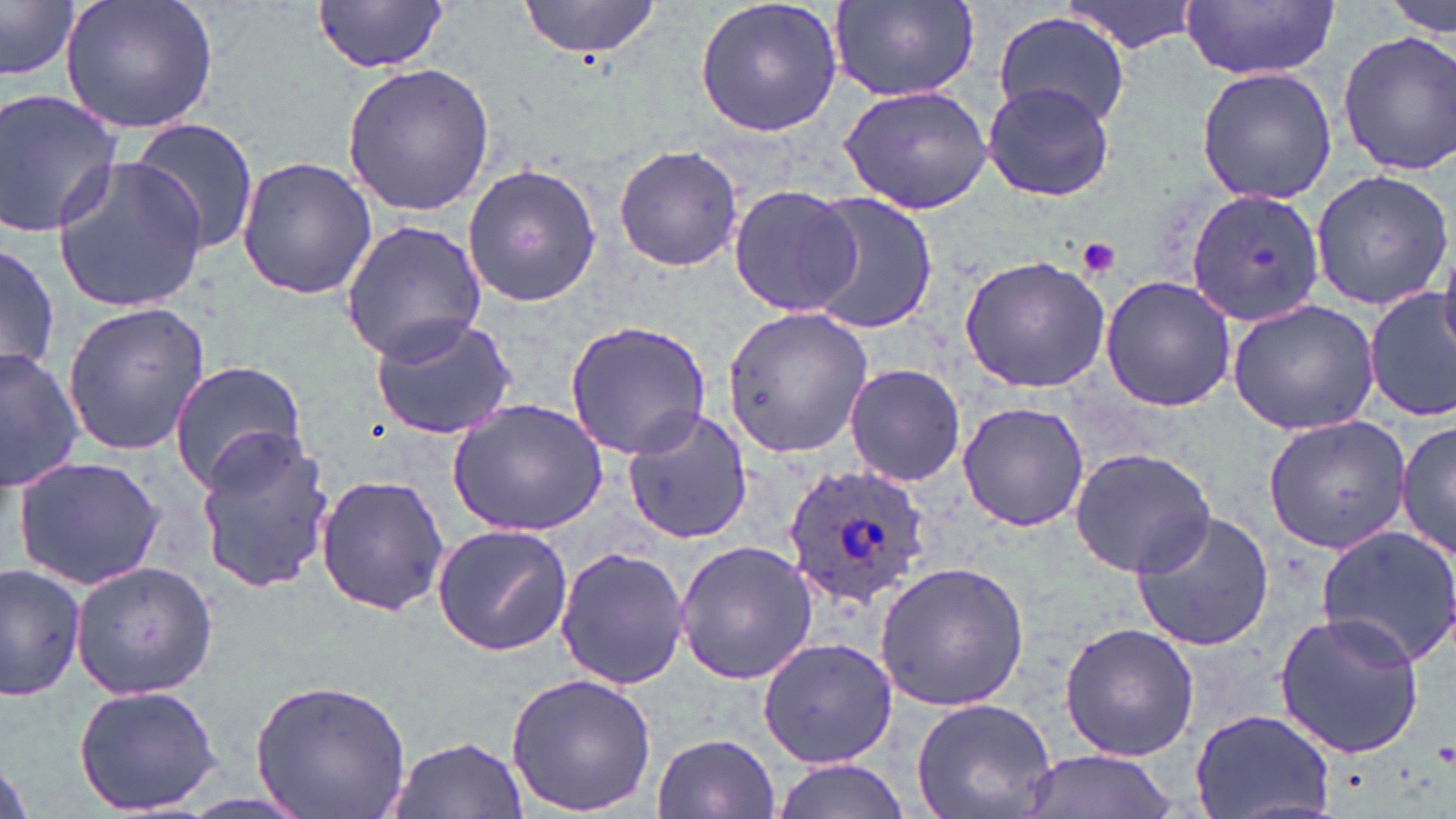 Approximate bounding boxes as (x1, y1, x2, y2) in pixels. Platelet locations: (1077, 237, 1120, 278), (1433, 741, 1456, 768). Uninfected red blood cell locations: (59, 0, 220, 137), (313, 0, 451, 73), (516, 0, 671, 58), (693, 0, 844, 139), (1063, 0, 1200, 54), (1181, 0, 1342, 79), (1384, 0, 1453, 39), (0, 1, 81, 82), (828, 1, 979, 104), (992, 10, 1132, 130), (1337, 32, 1456, 175), (341, 62, 494, 216), (1195, 65, 1335, 205), (839, 78, 997, 215), (982, 81, 1113, 202), (0, 87, 127, 239), (124, 119, 261, 259), (613, 146, 743, 273), (50, 155, 209, 314), (236, 155, 378, 301), (462, 164, 601, 309), (1310, 168, 1454, 312), (727, 185, 861, 317), (1187, 185, 1326, 325), (797, 191, 937, 333), (338, 220, 487, 364), (0, 240, 60, 382), (1436, 248, 1456, 359), (959, 255, 1110, 394), (1100, 277, 1238, 412), (1364, 289, 1455, 423), (1225, 298, 1382, 435), (61, 302, 211, 456), (720, 307, 874, 458), (369, 313, 520, 439), (563, 319, 712, 460), (0, 346, 84, 492), (169, 359, 307, 491), (843, 363, 967, 487), (447, 399, 607, 537), (957, 403, 1091, 532), (619, 408, 752, 548), (1263, 414, 1411, 553), (1397, 416, 1454, 566), (192, 428, 336, 591), (1069, 447, 1215, 575), (12, 455, 167, 591), (315, 474, 449, 617), (1129, 511, 1276, 654), (1313, 520, 1456, 669), (431, 525, 572, 654), (673, 540, 817, 686), (555, 548, 691, 692), (875, 560, 1030, 712), (1, 562, 86, 701), (71, 562, 217, 699), (1273, 611, 1427, 759), (1058, 623, 1200, 763), (758, 637, 897, 768), (505, 672, 658, 817), (251, 677, 412, 819), (74, 683, 223, 814), (911, 698, 1058, 819), (1189, 705, 1335, 819), (652, 732, 780, 818), (385, 734, 526, 819), (1019, 748, 1184, 818), (769, 759, 914, 819). Plasmodium ovale-infected red blood cell locations: (783, 462, 933, 610). Slide-level diagnosis: Plasmodium ovale. One field of a larger specimen. Image is 1456×819 pixels. May-Grünwald-Giemsa-stained preparation. Captured at 1000x magnification. Optical microscopy. Thin blood film.